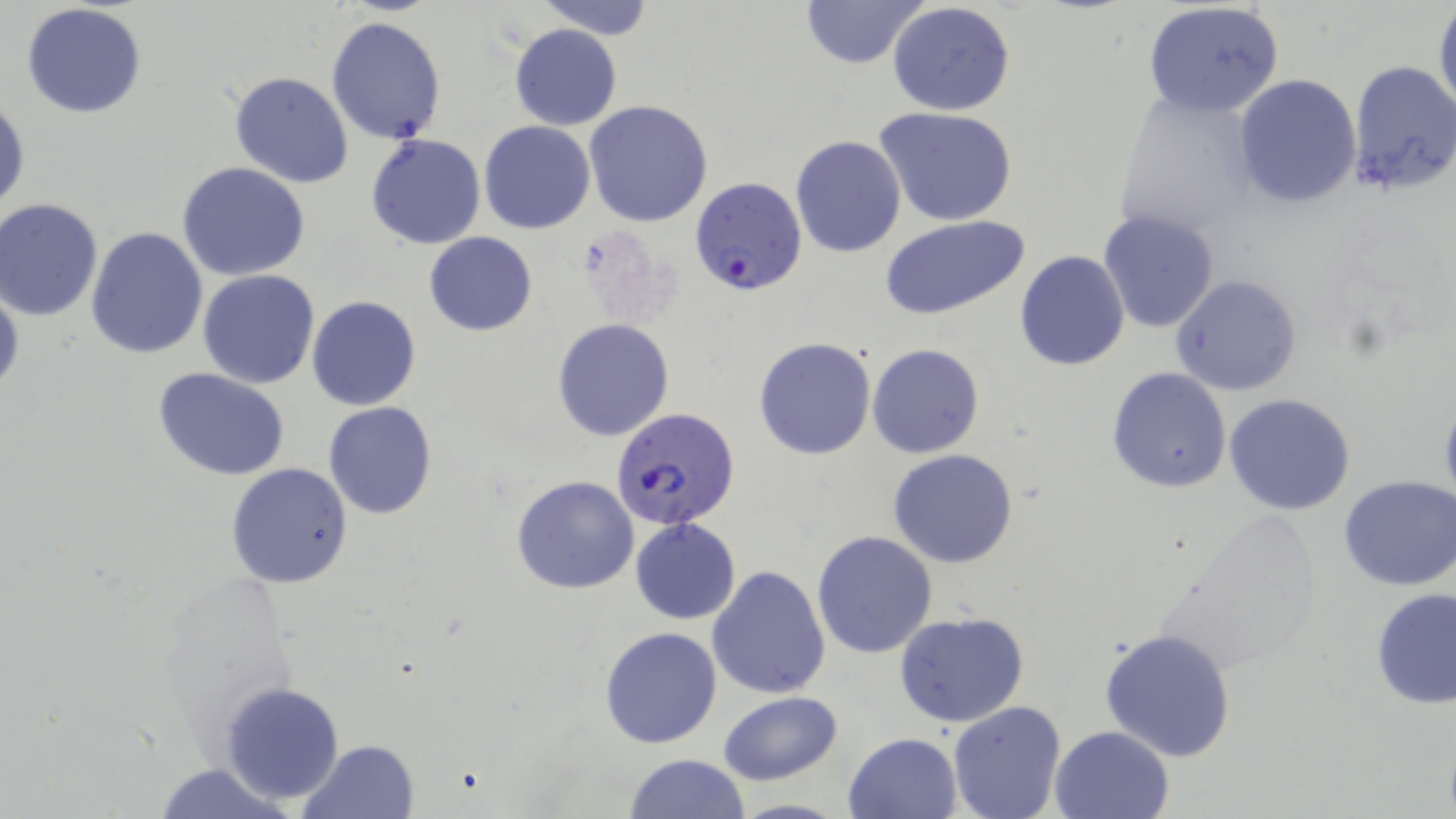
Approximate bounding boxes as named x1/y1/x2/y2 corners in pixels. Uninfected red blood cell locations: (x1=531, y1=0, x2=658, y2=40), (x1=800, y1=0, x2=927, y2=70), (x1=1141, y1=1, x2=1286, y2=119), (x1=886, y1=2, x2=1016, y2=117), (x1=21, y1=3, x2=148, y2=118), (x1=1433, y1=3, x2=1455, y2=120), (x1=326, y1=16, x2=446, y2=145), (x1=508, y1=24, x2=622, y2=130), (x1=1347, y1=59, x2=1456, y2=196), (x1=229, y1=72, x2=354, y2=189), (x1=1233, y1=75, x2=1361, y2=208), (x1=1111, y1=88, x2=1263, y2=240), (x1=1, y1=95, x2=29, y2=220), (x1=583, y1=100, x2=714, y2=227), (x1=874, y1=106, x2=1021, y2=228), (x1=480, y1=121, x2=596, y2=233), (x1=366, y1=135, x2=486, y2=250), (x1=791, y1=135, x2=906, y2=257), (x1=177, y1=163, x2=309, y2=281), (x1=0, y1=200, x2=103, y2=321), (x1=1098, y1=209, x2=1218, y2=332), (x1=880, y1=215, x2=1033, y2=321), (x1=85, y1=225, x2=209, y2=361), (x1=424, y1=232, x2=537, y2=335), (x1=1014, y1=250, x2=1130, y2=371), (x1=197, y1=270, x2=321, y2=389), (x1=1170, y1=273, x2=1302, y2=396), (x1=0, y1=277, x2=24, y2=401), (x1=306, y1=295, x2=421, y2=411), (x1=551, y1=319, x2=674, y2=441), (x1=754, y1=337, x2=875, y2=460), (x1=867, y1=344, x2=984, y2=458), (x1=1107, y1=367, x2=1232, y2=493), (x1=154, y1=368, x2=292, y2=481), (x1=1225, y1=393, x2=1356, y2=515), (x1=1437, y1=395, x2=1456, y2=517), (x1=323, y1=401, x2=438, y2=520), (x1=889, y1=449, x2=1019, y2=567), (x1=225, y1=462, x2=354, y2=589), (x1=511, y1=474, x2=640, y2=593), (x1=1338, y1=475, x2=1456, y2=591), (x1=629, y1=519, x2=742, y2=624), (x1=811, y1=530, x2=938, y2=659), (x1=707, y1=565, x2=832, y2=700), (x1=1371, y1=588, x2=1456, y2=709), (x1=896, y1=610, x2=1029, y2=728), (x1=599, y1=627, x2=721, y2=748), (x1=1098, y1=627, x2=1238, y2=763), (x1=218, y1=681, x2=347, y2=805), (x1=719, y1=691, x2=843, y2=783), (x1=947, y1=700, x2=1067, y2=819), (x1=1049, y1=725, x2=1173, y2=819), (x1=844, y1=733, x2=963, y2=819), (x1=297, y1=739, x2=421, y2=819), (x1=623, y1=754, x2=752, y2=818), (x1=150, y1=762, x2=300, y2=819). Plasmodium falciparum-infected red blood cell locations: (x1=693, y1=179, x2=809, y2=298), (x1=612, y1=412, x2=742, y2=530). Slide-level diagnosis: Plasmodium falciparum. May-Grünwald-Giemsa-stained preparation. Thin blood film. Light microscopy. Image is 1456×819 pixels. Single field of view. Captured at 1000x magnification.